Report the malaria status of this cell.
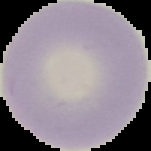
It is uninfected.

Summary:
  - Image type: segmented cell region on a black background
  - Image size: 151×151 pixels
  - Preparation: thin blood film